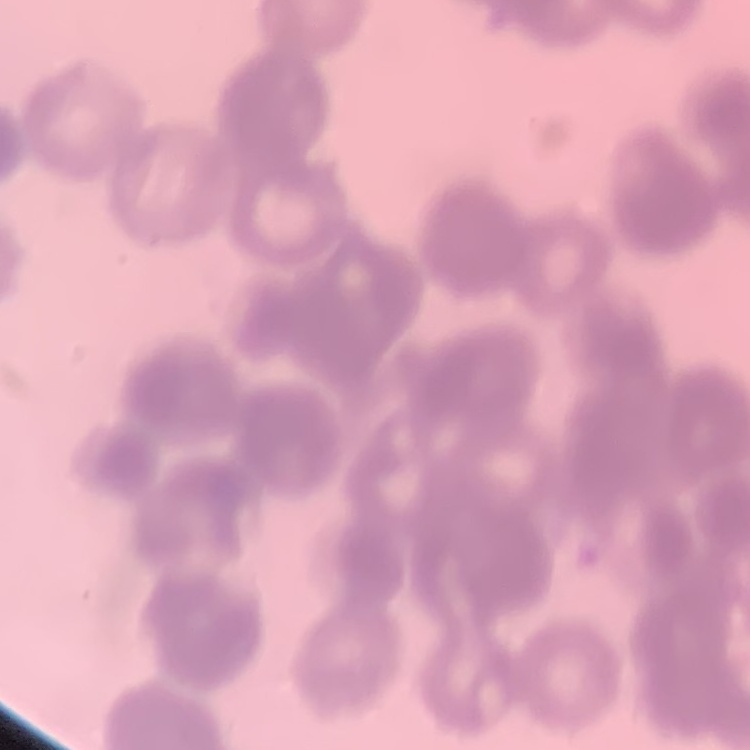
Summary:
  - Red blood cell morphology: rouleaux formation
  - Stain: Field's or Giemsa
  - Image type: square crop of a larger photomicrograph
  - Preparation: thin blood smear